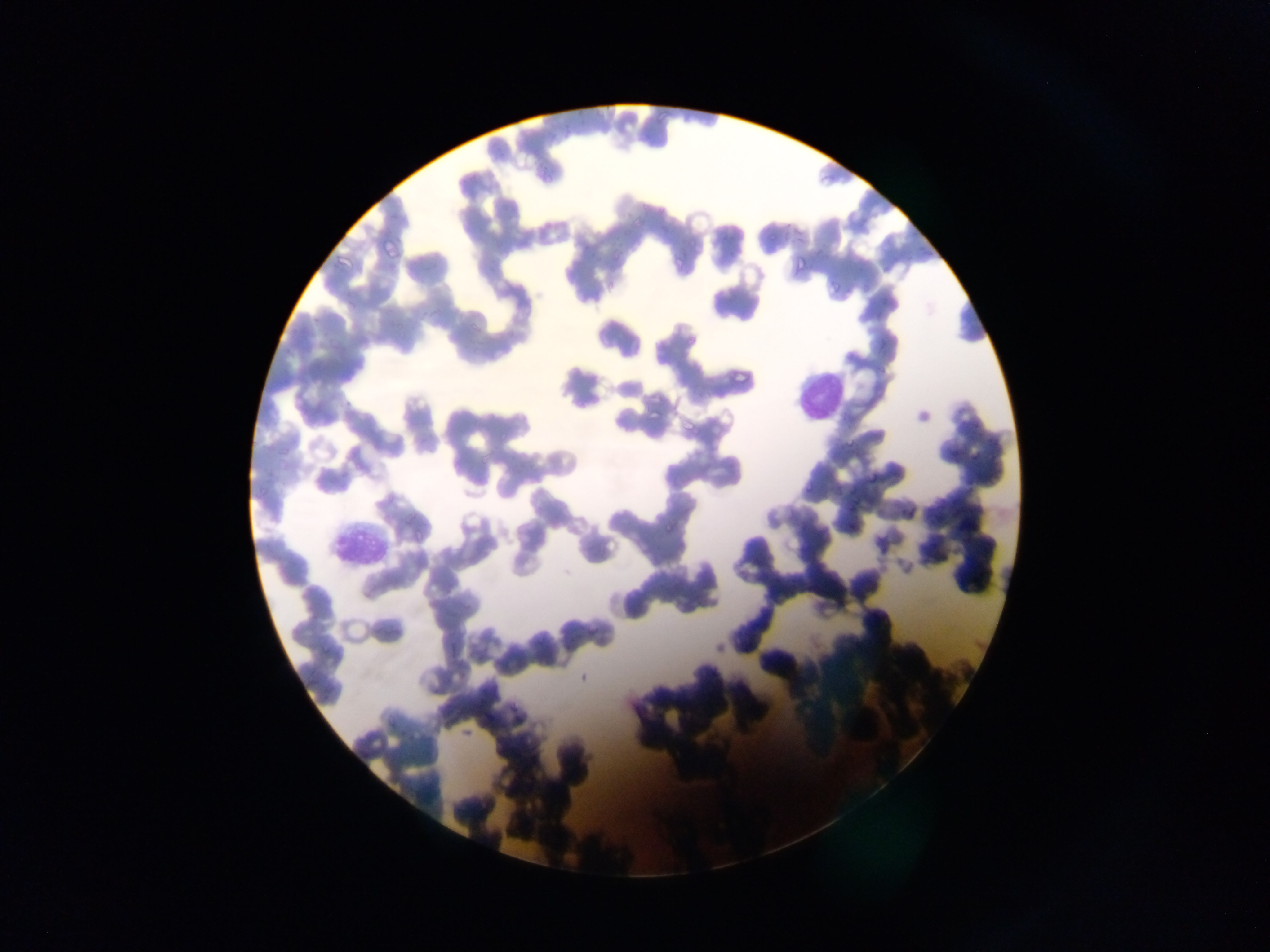
Approximate bounding boxes as (left, top, right, bottom) in pixels. Plasmodium parasite locations: (537, 167, 550, 176), (543, 175, 553, 184), (647, 408, 661, 419), (845, 437, 855, 446), (867, 472, 877, 483), (805, 483, 811, 494), (853, 494, 861, 503), (845, 506, 855, 510), (664, 523, 671, 531). Leukocyte locations: (791, 364, 848, 418), (330, 526, 387, 564). Photographed through a microscope with a mobile-phone camera. Single field of view. Image is 1270×952 pixels. Thin blood smear. Sample from Ghana.